Name the cell type shown.
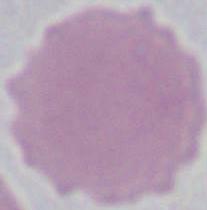
An erythrocyte.

1000x magnification. Micrograph.